Assess this cell for malaria.
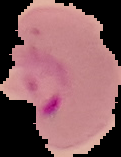

Parasitized.

Segmented cell region on a black background. From a thin blood film. Image is 121×157 pixels.